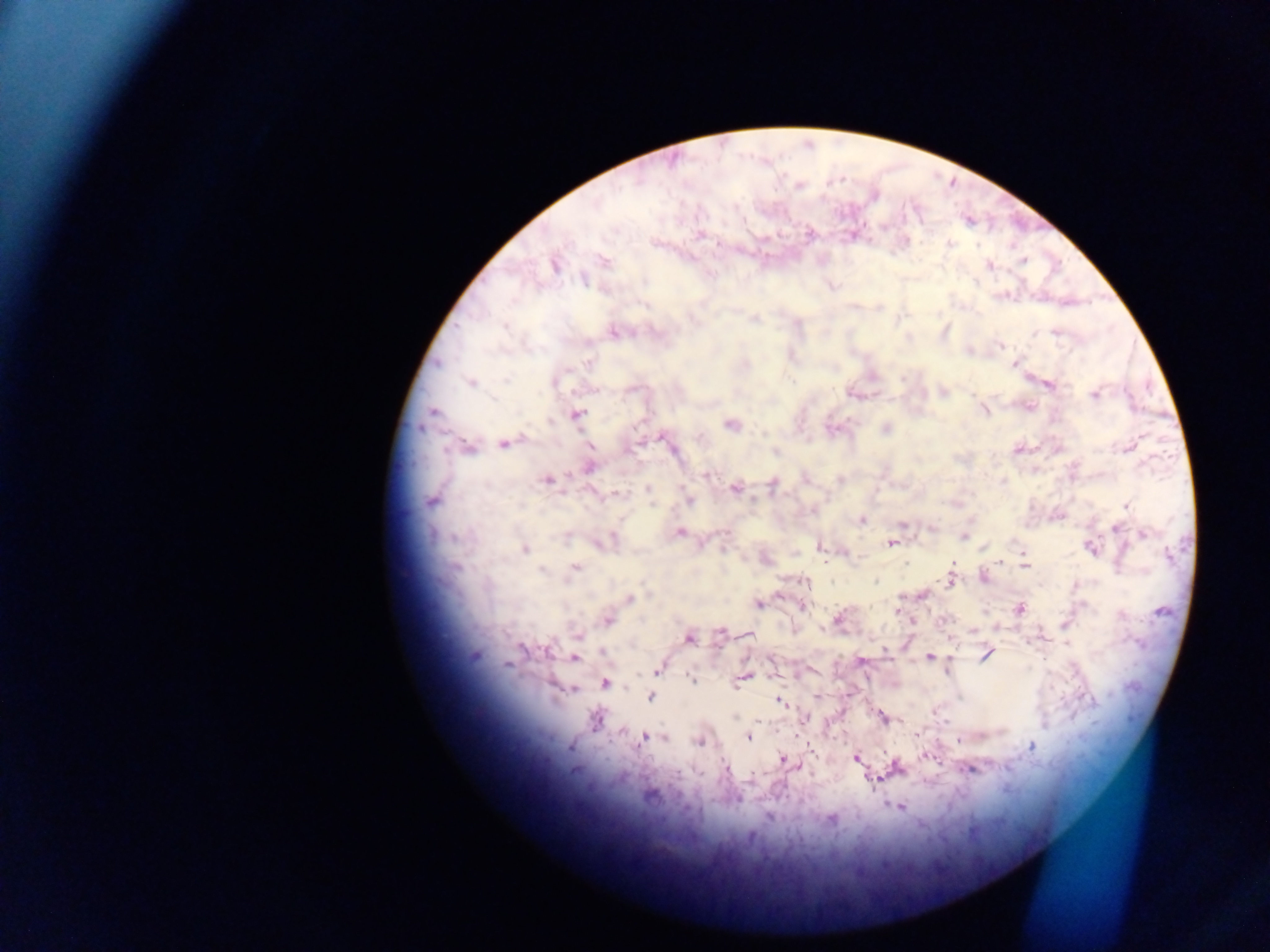

Approximate centers as {x, y} in pixels. Plasmodium parasite locations: {699, 237}, {950, 243}, {605, 262}, {554, 265}, {990, 265}, {583, 280}, {755, 319}, {505, 327}, {615, 333}, {437, 363}, {1014, 364}, {506, 380}, {793, 381}, {471, 383}, {554, 383}, {1049, 385}, {1094, 395}, {985, 411}, {433, 412}, {578, 415}, {550, 421}, {731, 425}, {886, 429}, {661, 438}, {503, 444}, {468, 448}, {776, 452}, {589, 468}, {707, 475}, {548, 479}, {840, 479}, {772, 485}, {647, 488}, {735, 489}, {617, 494}, {689, 500}, {431, 501}, {1126, 506}, {862, 520}, {902, 525}, {1116, 529}, {680, 532}, {1143, 534}, {455, 537}, {964, 537}, {890, 544}, {821, 548}, {1090, 548}, {525, 549}, {1023, 554}, {1000, 561}, {953, 563}, {1025, 565}, {457, 567}, {575, 567}, {542, 571}, {949, 580}, {876, 581}, {806, 582}, {629, 598}, {759, 604}, {802, 606}, {1019, 609}, {897, 611}, {838, 618}, {608, 621}, {720, 633}, {747, 634}, {577, 636}, {689, 639}, {523, 648}, {885, 650}, {548, 652}, {603, 652}, {986, 655}, {929, 657}, {576, 659}, {860, 660}, {507, 665}, {657, 670}, {743, 677}, {692, 679}, {739, 681}, {605, 684}, {736, 686}, {574, 689}, {816, 696}, {651, 698}, {780, 701}, {735, 717}, {806, 718}, {884, 718}, {595, 720}, {758, 721}, {917, 733}, {664, 737}, {748, 737}, {643, 738}, {960, 740}, {699, 743}, {1031, 746}, {812, 751}, {928, 757}, {856, 759}, {783, 760}, {795, 765}, {725, 766}, {970, 770}, {875, 778}, {900, 808}, {768, 817}. Collected in Ghana. Image is 1270×952 pixels. Thick blood smear. Mobile-phone photograph taken through the microscope. One field of view.